Report the malaria status of this cell.
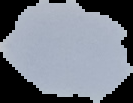
Uninfected.

From a thin blood film. Segmented cell region on a black background. Image is 133×103 pixels.